Assess this cell for malaria.
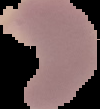
Parasitized.

Summary:
  - Image size: 100×109 pixels
  - Image type: cell region segmented out of the field of view; surrounding area masked to black
  - Preparation: thin blood smear